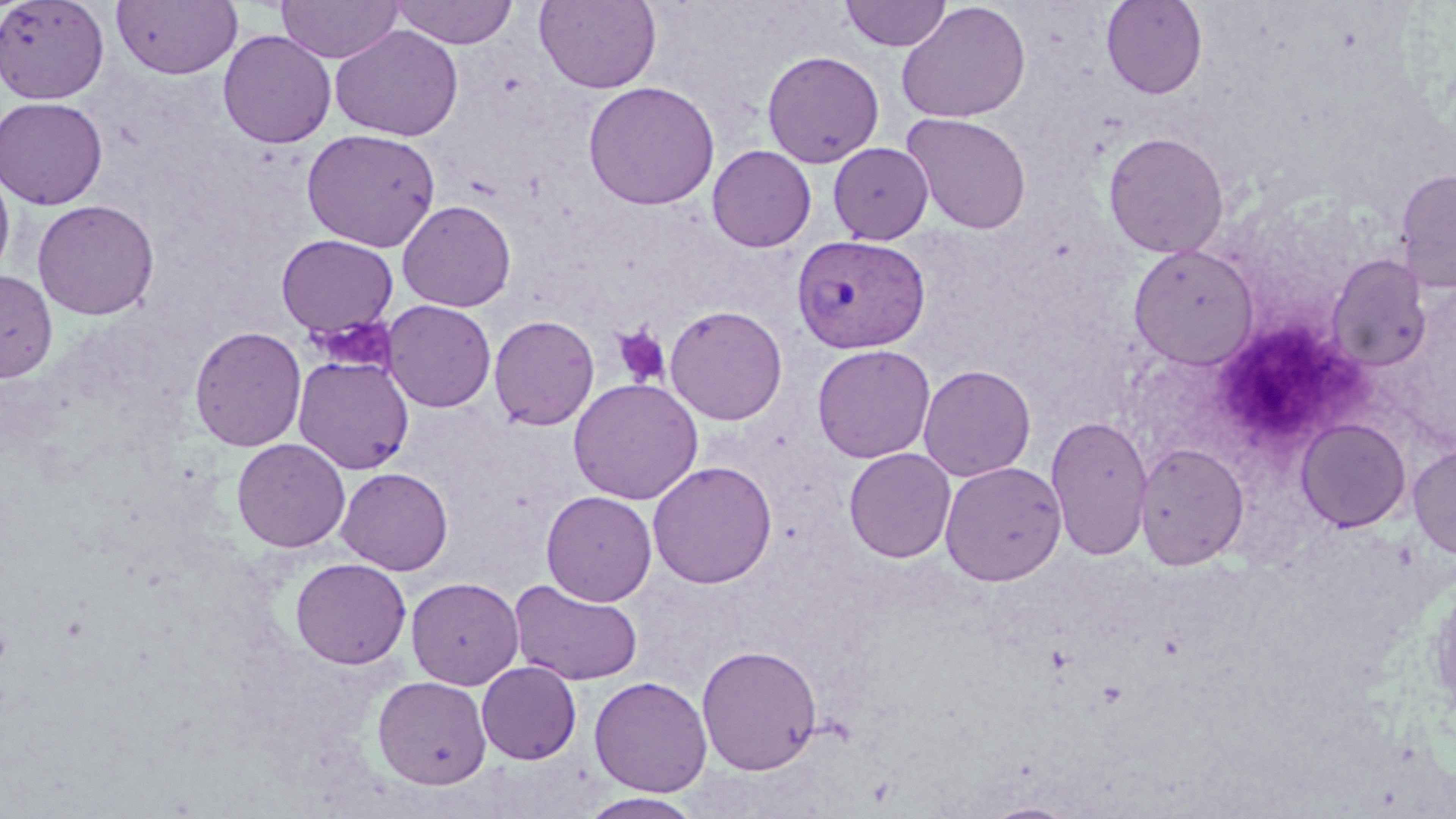 Approximate bounding boxes as named x1/y1/x2/y2 corners in pixels. Platelet locations: (x1=309, y1=315, x2=398, y2=375), (x1=1219, y1=321, x2=1355, y2=431), (x1=611, y1=324, x2=671, y2=387). Plasmodium vivax-infected red blood cell locations: (x1=792, y1=234, x2=931, y2=354). Uninfected red blood cell locations: (x1=0, y1=0, x2=110, y2=104), (x1=111, y1=0, x2=243, y2=80), (x1=275, y1=0, x2=406, y2=63), (x1=389, y1=0, x2=519, y2=49), (x1=534, y1=0, x2=662, y2=93), (x1=840, y1=0, x2=952, y2=52), (x1=1101, y1=0, x2=1207, y2=99), (x1=896, y1=2, x2=1031, y2=124), (x1=329, y1=24, x2=464, y2=141), (x1=218, y1=29, x2=336, y2=148), (x1=762, y1=50, x2=885, y2=168), (x1=583, y1=80, x2=720, y2=210), (x1=0, y1=96, x2=108, y2=209), (x1=901, y1=113, x2=1032, y2=234), (x1=301, y1=128, x2=441, y2=252), (x1=1103, y1=131, x2=1230, y2=258), (x1=828, y1=142, x2=934, y2=245), (x1=706, y1=145, x2=816, y2=252), (x1=0, y1=165, x2=15, y2=283), (x1=1394, y1=168, x2=1456, y2=292), (x1=32, y1=199, x2=159, y2=320), (x1=397, y1=199, x2=517, y2=312), (x1=276, y1=234, x2=399, y2=338), (x1=1128, y1=244, x2=1260, y2=369), (x1=1327, y1=253, x2=1432, y2=372), (x1=0, y1=269, x2=58, y2=382), (x1=383, y1=299, x2=496, y2=412), (x1=664, y1=305, x2=788, y2=425), (x1=489, y1=314, x2=599, y2=430), (x1=189, y1=325, x2=307, y2=451), (x1=812, y1=344, x2=936, y2=463), (x1=293, y1=355, x2=414, y2=474), (x1=918, y1=364, x2=1036, y2=482), (x1=567, y1=377, x2=704, y2=505), (x1=1045, y1=414, x2=1153, y2=561), (x1=1295, y1=417, x2=1412, y2=532), (x1=231, y1=438, x2=350, y2=552), (x1=1135, y1=441, x2=1250, y2=570), (x1=1408, y1=443, x2=1456, y2=560), (x1=843, y1=448, x2=956, y2=563), (x1=647, y1=460, x2=777, y2=588), (x1=939, y1=461, x2=1066, y2=585), (x1=336, y1=467, x2=453, y2=575), (x1=541, y1=490, x2=657, y2=605), (x1=290, y1=558, x2=411, y2=670), (x1=406, y1=577, x2=524, y2=689), (x1=510, y1=579, x2=643, y2=685), (x1=696, y1=643, x2=822, y2=774), (x1=476, y1=662, x2=581, y2=764), (x1=372, y1=675, x2=492, y2=789), (x1=589, y1=675, x2=712, y2=796), (x1=578, y1=792, x2=705, y2=819), (x1=979, y1=801, x2=1081, y2=819). Slide-level diagnosis: Plasmodium vivax. Optical microscopy. Thin blood film. May-Grünwald-Giemsa-stained preparation. 1000x magnification. One field of a larger specimen. Image is 1456×819 pixels.